Report the malaria status of this cell.
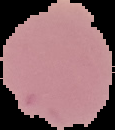
It is uninfected.

Segmented cell region on a black background. From a thin blood film. Image is 115×130 pixels.